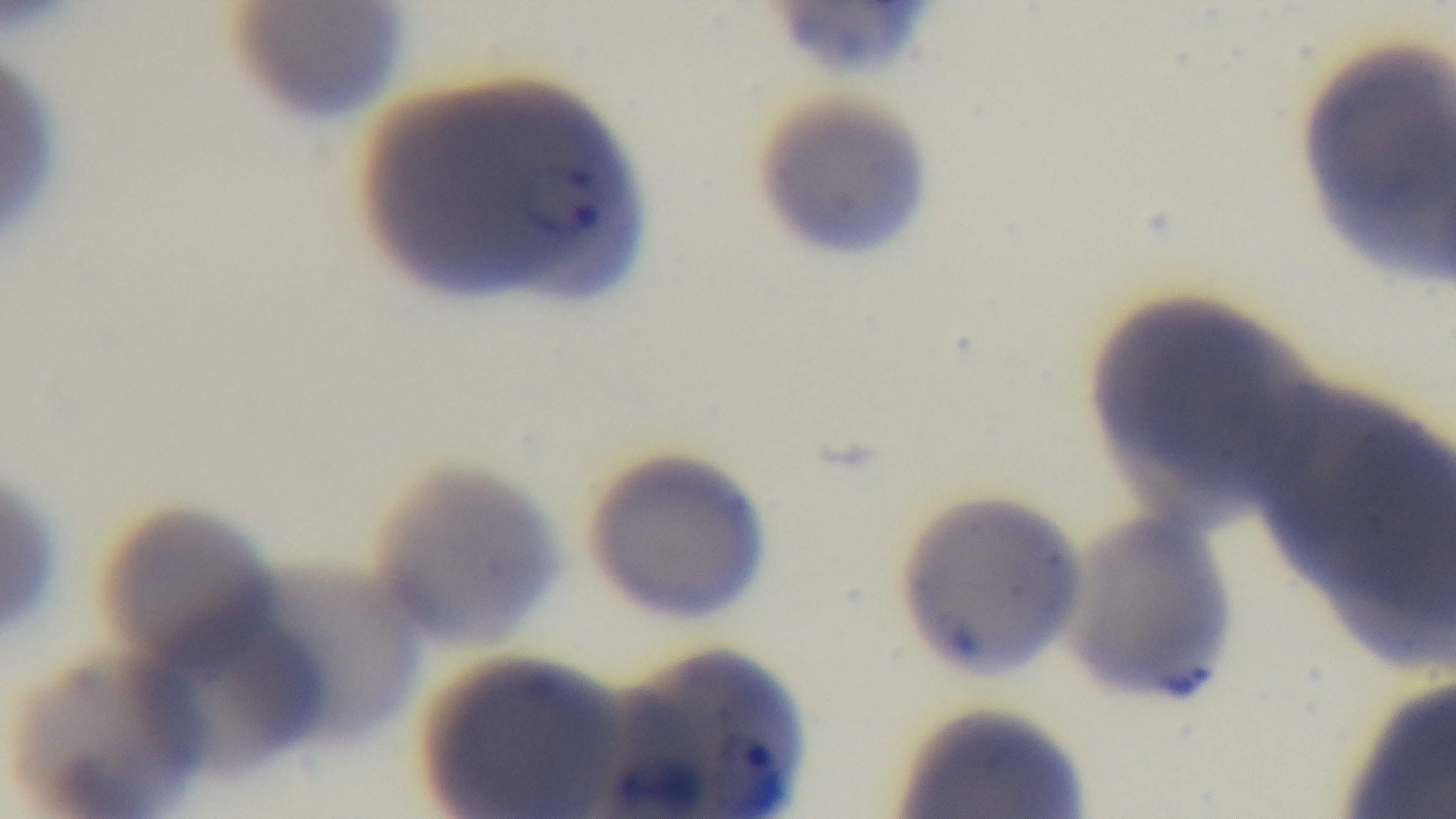

capture = mounted 4K digital camera
malaria status = positive
field of view = single
modality = light microscopy
objective = 100x oil immersion
stain = Giemsa
preparation = thin